Identify the blood parasite species.
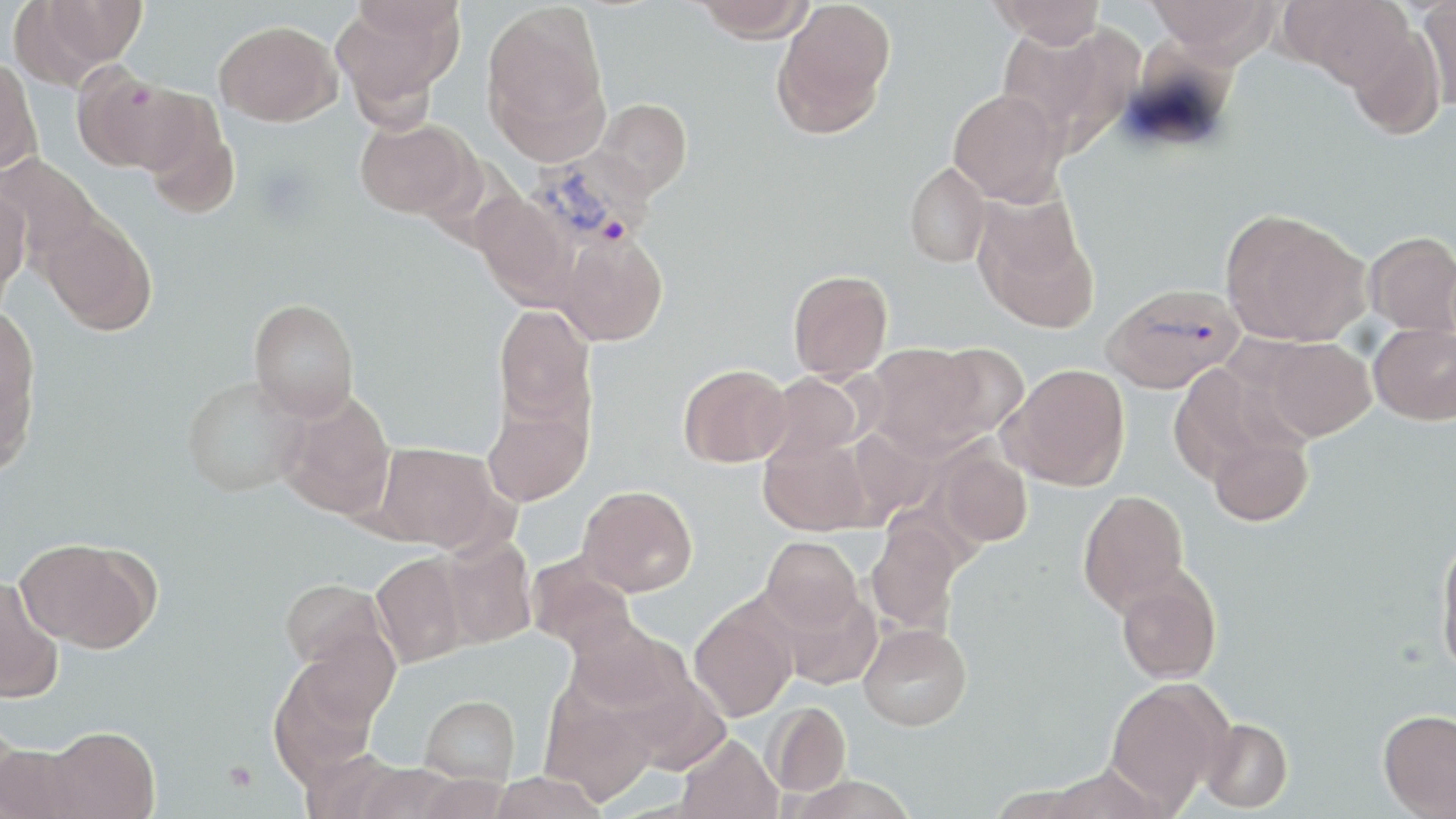
Plasmodium vivax.

platelet_locations: 'approximate bounding boxes as [x1, y1, x2, y2] in pixels: [222, 761, 258, 794]'
modality: light microscopy
uninfected_red_blood_cell_locations: 'approximate bounding boxes as [x1, y1, x2, y2] in pixels: [42, 0, 147, 66], [331, 0, 461, 117], [693, 0, 815, 41], [990, 0, 1106, 47], [1146, 0, 1277, 63], [1289, 0, 1413, 88], [1419, 0, 1456, 112], [9, 1, 122, 89], [771, 1, 896, 137], [482, 3, 609, 148], [214, 20, 341, 126], [997, 24, 1122, 146], [1346, 24, 1446, 140], [0, 57, 43, 178], [74, 66, 199, 175], [948, 88, 1066, 205], [595, 98, 692, 198], [139, 103, 240, 219], [354, 117, 477, 220], [0, 154, 106, 267], [904, 162, 990, 267], [0, 183, 30, 305], [471, 192, 578, 306], [972, 194, 1099, 332], [1220, 208, 1371, 346], [38, 214, 157, 335], [553, 231, 668, 346], [1365, 232, 1456, 335], [788, 269, 893, 381], [248, 298, 359, 421], [494, 304, 596, 432], [0, 307, 40, 471], [1369, 322, 1456, 425], [1259, 337, 1376, 441], [866, 343, 985, 456], [931, 343, 1030, 439], [679, 363, 791, 467], [1003, 363, 1130, 491], [1169, 364, 1288, 484], [762, 372, 865, 465], [182, 375, 307, 497], [277, 391, 396, 520], [482, 399, 592, 507], [1207, 430, 1313, 527], [759, 434, 872, 536], [374, 442, 499, 552], [937, 445, 1032, 549], [577, 485, 698, 596], [1077, 489, 1189, 614], [866, 520, 963, 635], [761, 535, 862, 632], [1435, 536, 1456, 677], [436, 537, 537, 649], [16, 538, 157, 653], [370, 551, 471, 667], [526, 554, 637, 656], [1116, 566, 1222, 684], [0, 576, 64, 702], [280, 578, 390, 676], [777, 586, 882, 691], [689, 598, 799, 722], [565, 618, 687, 718], [858, 623, 972, 731], [288, 626, 400, 734], [1104, 678, 1229, 811], [540, 687, 659, 805], [420, 695, 519, 783], [765, 701, 851, 796], [1378, 708, 1456, 818], [1199, 718, 1293, 813], [45, 725, 160, 819], [677, 734, 782, 819], [0, 742, 86, 818], [352, 763, 463, 819], [1045, 764, 1161, 818], [489, 771, 607, 819]'
stain: May-Grünwald-Giemsa
magnification: 1000x
field_of_view: one of a larger specimen
plasmodium_vivax_infected_red_blood_cell_locations: 'approximate bounding boxes as [x1, y1, x2, y2] in pixels: [531, 150, 658, 252], [1103, 282, 1245, 393]'
preparation: thin blood smear
image_size: 1456×819 pixels